Identify the blood parasite species.
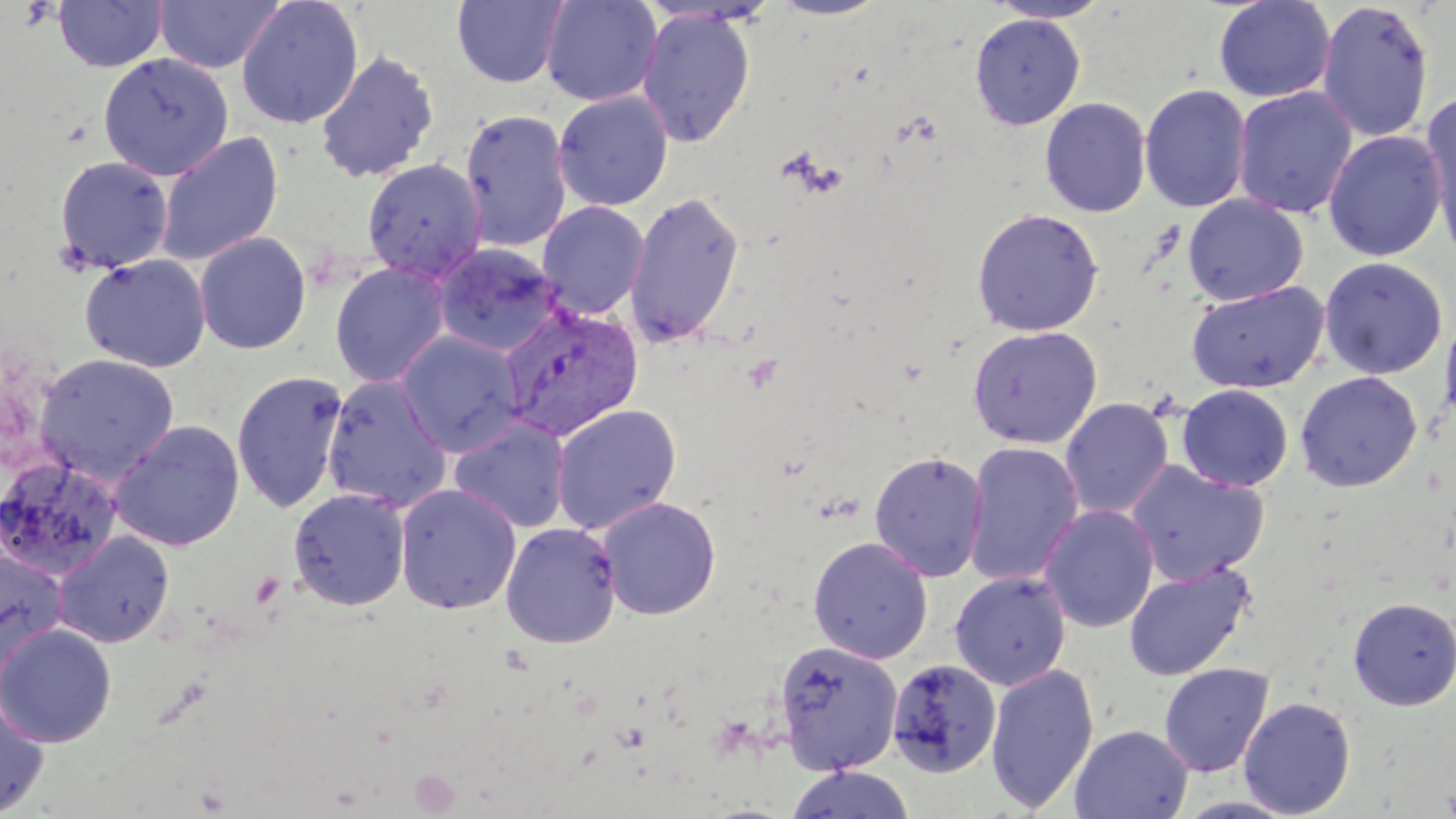
Plasmodium vivax.

Summary:
  - Coordinate format: approximate bounding boxes as (x1,y1)-(x2,y2) corner pairs in pixels
  - Uninfected red blood cell locations: (154,0)-(285,73), (236,0)-(364,129), (451,0)-(570,88), (540,0)-(663,107), (768,0)-(889,20), (1213,0)-(1336,103), (52,1)-(169,73), (986,1)-(1115,23), (1316,2)-(1434,142), (636,8)-(756,147), (970,13)-(1085,130), (315,49)-(439,183), (98,53)-(234,180), (1139,84)-(1252,213), (1233,87)-(1357,219), (552,90)-(673,211), (1420,92)-(1456,256), (1040,97)-(1151,218), (459,109)-(573,252), (154,131)-(284,267), (1323,131)-(1447,261), (53,155)-(173,274), (361,158)-(487,283), (624,190)-(745,348), (1183,194)-(1308,306), (537,201)-(649,319), (971,208)-(1104,336), (193,231)-(312,354), (432,242)-(564,358), (78,253)-(212,372), (1319,257)-(1448,379), (329,261)-(452,388), (1186,281)-(1329,394), (1439,307)-(1456,431), (966,325)-(1103,449), (395,330)-(526,457), (34,352)-(180,484), (232,371)-(348,514), (1295,371)-(1423,492), (322,374)-(454,513), (1177,384)-(1293,492), (1060,397)-(1174,519), (550,403)-(682,534), (448,417)-(573,533), (109,419)-(246,551), (962,441)-(1084,587), (869,451)-(988,582), (0,456)-(125,580), (1126,461)-(1269,585), (394,482)-(523,615), (288,487)-(411,611), (596,496)-(721,620), (1039,505)-(1159,633), (501,522)-(622,649), (52,531)-(175,648), (808,536)-(933,663), (0,547)-(69,679), (1123,561)-(1256,682), (950,571)-(1072,690), (1348,596)-(1456,710), (0,622)-(117,747), (773,639)-(903,774), (887,659)-(1001,778), (985,663)-(1100,813), (1159,663)-(1273,777), (0,695)-(51,817), (1238,697)-(1356,818), (1070,725)-(1193,819), (784,765)-(916,819), (1172,795)-(1301,818)
  - Plasmodium vivax-infected red blood cell locations: (499,302)-(644,441)
  - Preparation: thin blood film
  - Field of view: single
  - Image size: 1456×819 pixels
  - Stain: May-Grünwald-Giemsa
  - Magnification: 1000x
  - Modality: light microscopy